Locate every Plasmodium ovale-infected red blood cell.
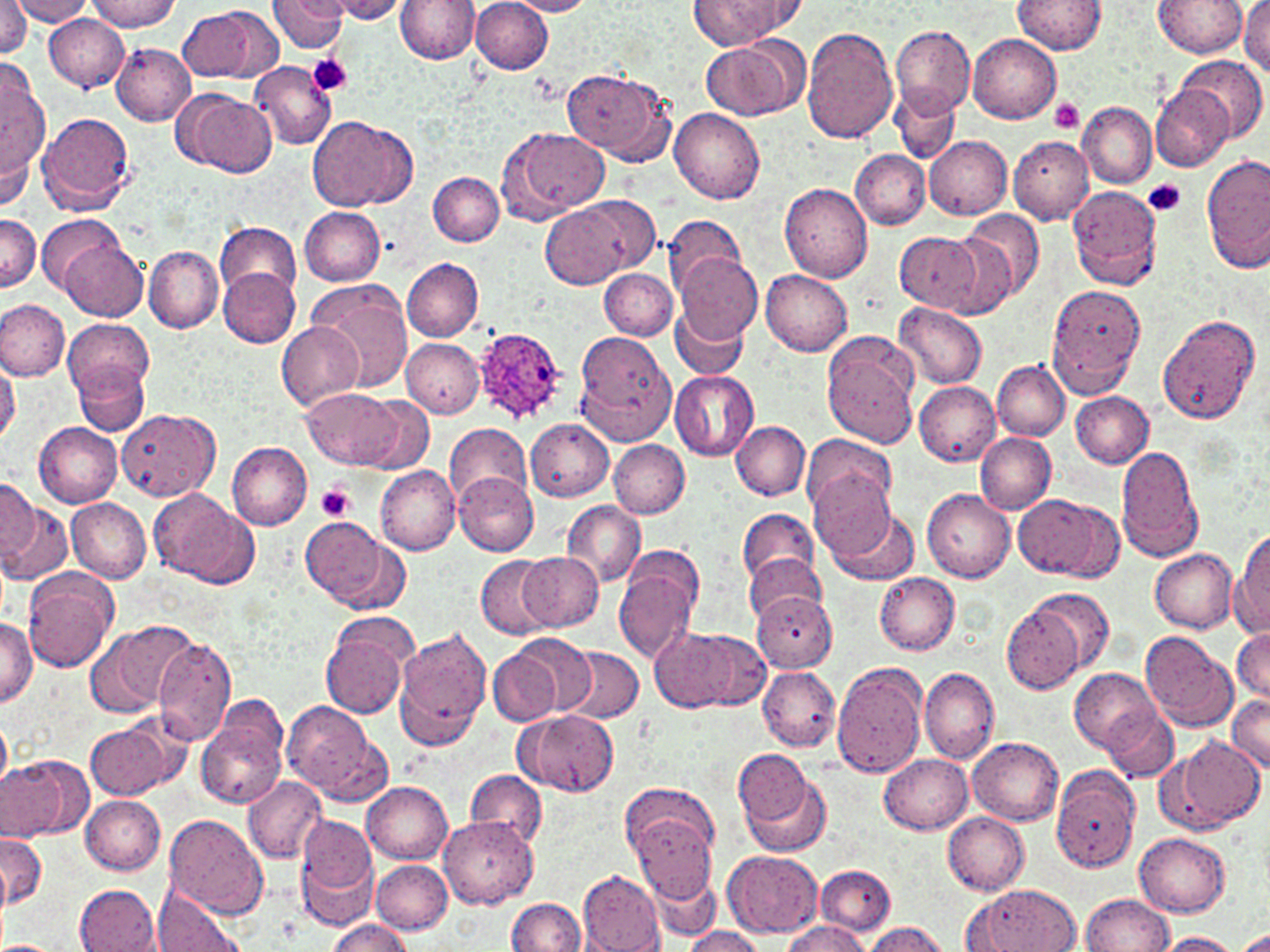
Approximate bounding boxes as [x1, y1, x2, y2] in pixels.
Plasmodium ovale-infected red blood cells: [472, 325, 571, 427].

Summary:
  - Platelet locations: [307, 54, 353, 97], [1050, 99, 1085, 134], [1144, 178, 1186, 216], [316, 483, 355, 521]
  - Uninfected red blood cell locations: [1, 0, 31, 58], [12, 0, 94, 25], [85, 0, 181, 31], [325, 0, 412, 23], [395, 0, 479, 64], [470, 0, 552, 73], [507, 0, 596, 16], [1012, 0, 1107, 55], [1153, 0, 1247, 57], [1238, 0, 1270, 77], [268, 1, 349, 54], [691, 1, 782, 47], [179, 6, 267, 84], [44, 14, 129, 92], [890, 24, 974, 119], [800, 26, 898, 143], [968, 35, 1061, 123], [700, 37, 805, 119], [112, 44, 196, 125], [1178, 55, 1267, 145], [251, 62, 337, 149], [562, 66, 673, 165], [1, 71, 49, 189], [1151, 85, 1233, 172], [891, 87, 961, 165], [174, 90, 276, 179], [1077, 103, 1156, 188], [670, 109, 765, 204], [37, 111, 136, 215], [307, 115, 415, 212], [502, 126, 610, 221], [925, 136, 1012, 220], [1009, 136, 1094, 224], [1, 146, 32, 215], [852, 150, 930, 229], [1202, 154, 1270, 272], [429, 173, 504, 246], [779, 183, 874, 283], [1067, 184, 1164, 289], [539, 197, 641, 290], [300, 207, 386, 286], [965, 210, 1044, 302], [0, 213, 40, 295], [663, 214, 744, 296], [38, 215, 125, 296], [216, 220, 303, 303], [896, 233, 984, 315], [934, 233, 1019, 318], [58, 237, 148, 321], [144, 246, 223, 333], [675, 252, 762, 345], [401, 256, 484, 341], [218, 268, 300, 347], [600, 268, 678, 341], [760, 270, 853, 356], [308, 278, 412, 394], [1045, 284, 1144, 396], [0, 298, 69, 380], [670, 303, 748, 381], [893, 303, 988, 388], [1157, 314, 1261, 425], [63, 317, 153, 407], [277, 322, 363, 410], [574, 332, 676, 445], [822, 333, 919, 449], [401, 338, 484, 418], [0, 355, 19, 444], [992, 361, 1069, 441], [73, 362, 149, 435], [669, 371, 760, 461], [914, 380, 1001, 466], [304, 389, 403, 470], [1071, 391, 1153, 468], [360, 396, 434, 471], [116, 409, 220, 499], [526, 419, 614, 501], [33, 421, 123, 508], [445, 421, 532, 508], [731, 421, 810, 500], [975, 432, 1055, 513], [802, 434, 896, 523], [610, 440, 688, 518], [226, 442, 312, 530], [1116, 446, 1202, 562], [375, 465, 460, 555], [809, 469, 896, 561], [454, 473, 539, 555], [0, 477, 48, 571], [149, 489, 258, 588], [923, 489, 1017, 583], [1014, 494, 1112, 579], [66, 497, 151, 583], [561, 500, 644, 588], [2, 501, 70, 587], [825, 504, 919, 586], [738, 508, 819, 592], [301, 515, 389, 606], [1233, 533, 1270, 635], [333, 538, 409, 615], [613, 550, 705, 661], [1150, 550, 1237, 633], [519, 551, 603, 634], [742, 553, 825, 624], [475, 556, 554, 638], [23, 571, 119, 671], [874, 572, 960, 656], [1029, 588, 1115, 677], [752, 591, 837, 671], [1001, 603, 1084, 693], [0, 616, 37, 706], [319, 619, 413, 717], [89, 620, 199, 719], [394, 626, 492, 749], [650, 626, 748, 713], [1233, 626, 1270, 706], [1140, 630, 1238, 731], [689, 631, 770, 708], [506, 632, 596, 718], [153, 637, 236, 743], [487, 646, 564, 726], [559, 647, 644, 724], [831, 660, 928, 778], [757, 666, 841, 752], [1071, 667, 1162, 752], [920, 668, 999, 764], [1226, 694, 1270, 774], [282, 700, 384, 800], [198, 703, 289, 810], [1103, 707, 1177, 782], [518, 709, 617, 797], [0, 714, 11, 793], [86, 719, 179, 800], [1173, 736, 1263, 831], [969, 737, 1064, 827], [734, 748, 811, 827], [880, 753, 973, 832], [2, 757, 80, 840], [736, 766, 831, 860], [1057, 767, 1141, 873], [467, 770, 547, 847], [241, 776, 326, 864], [361, 781, 453, 864], [80, 795, 166, 874], [627, 798, 719, 901], [943, 812, 1029, 895], [166, 815, 267, 917], [296, 815, 378, 911], [438, 816, 537, 908], [0, 832, 47, 909], [1135, 833, 1230, 917], [724, 851, 823, 937], [370, 860, 451, 933], [815, 864, 896, 936], [643, 865, 721, 943], [577, 871, 665, 952], [74, 884, 161, 951], [967, 884, 1082, 952], [152, 887, 247, 952], [1080, 893, 1174, 951], [507, 897, 586, 951], [326, 919, 413, 952], [781, 920, 871, 951], [864, 922, 948, 952], [680, 928, 765, 952], [1238, 928, 1270, 951], [1155, 932, 1241, 952], [0, 941, 61, 952]
  - Slide-level diagnosis: Plasmodium ovale
  - Preparation: thin blood smear
  - Stain: May-Grünwald-Giemsa
  - Modality: optical microscopy
  - Image size: 1270×952 pixels
  - Magnification: 1000x
  - Field of view: one of a larger specimen